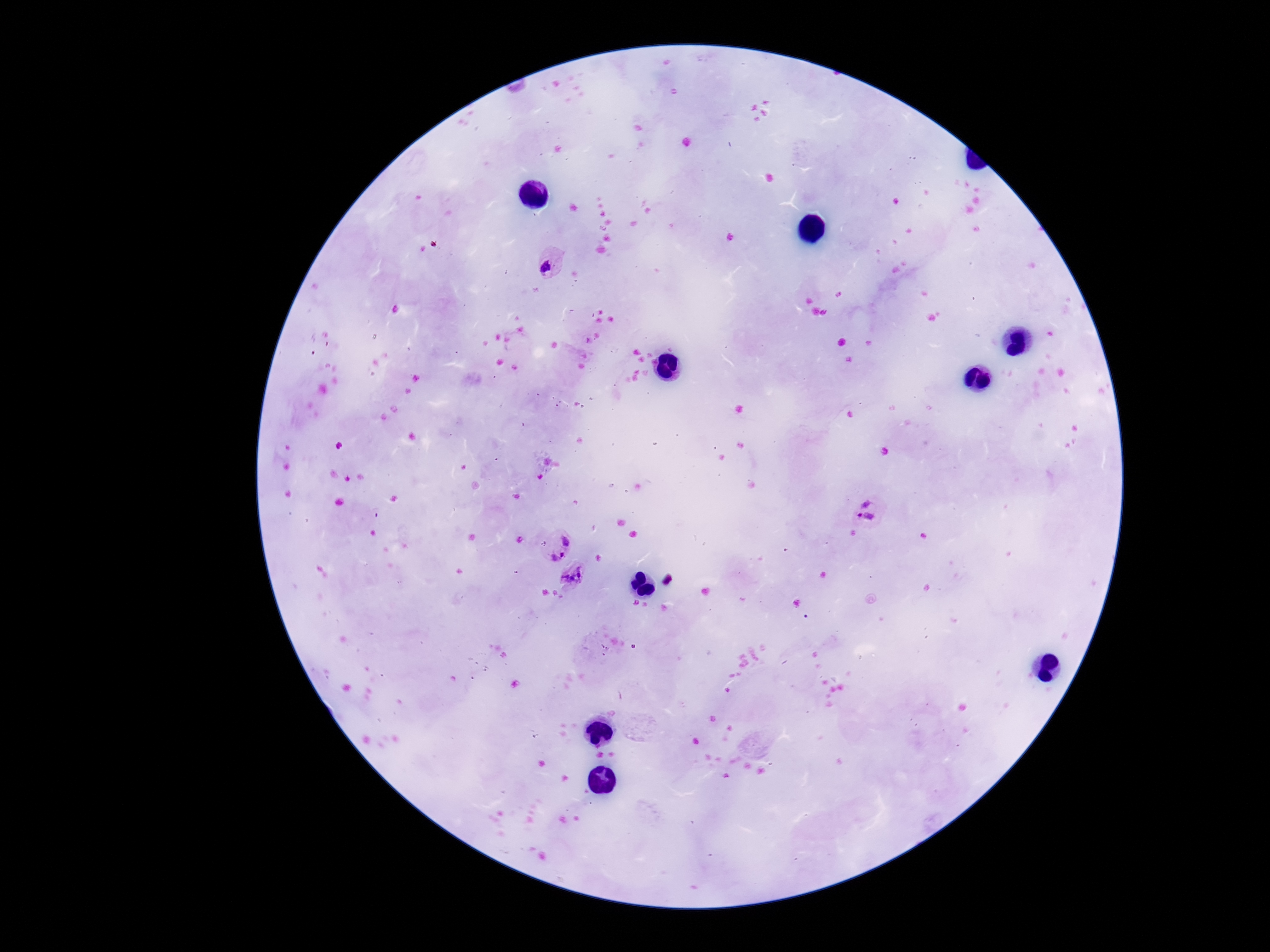

preparation = thick blood smear
stain = Giemsa
capture = smartphone camera through the microscope eyepiece
field of view = one from this slide
image size = 1270×952 pixels
patient malaria status = positive
Plasmodium parasite locations = approximate centers as {x, y} in pixels: {549, 268}, {867, 502}, {864, 522}, {566, 539}, {558, 559}, {573, 576}
magnification = 100x